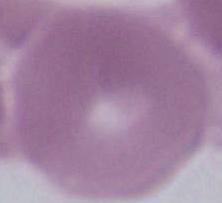
Photomicrograph. Captured at 1000x magnification. A red blood cell is seen.